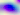

identification = Toxoplasma gondii
magnification = 400x
modality = photomicrograph